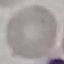 Malaria status: uninfected. Photographed with a smartphone camera at the microscope eyepiece. Automatically extracted cell patch, resized to 64 × 64 pixels. Giemsa stain. Thin smear of blood.